Give the extent of all Plasmodium falciparum-infected red blood cells.
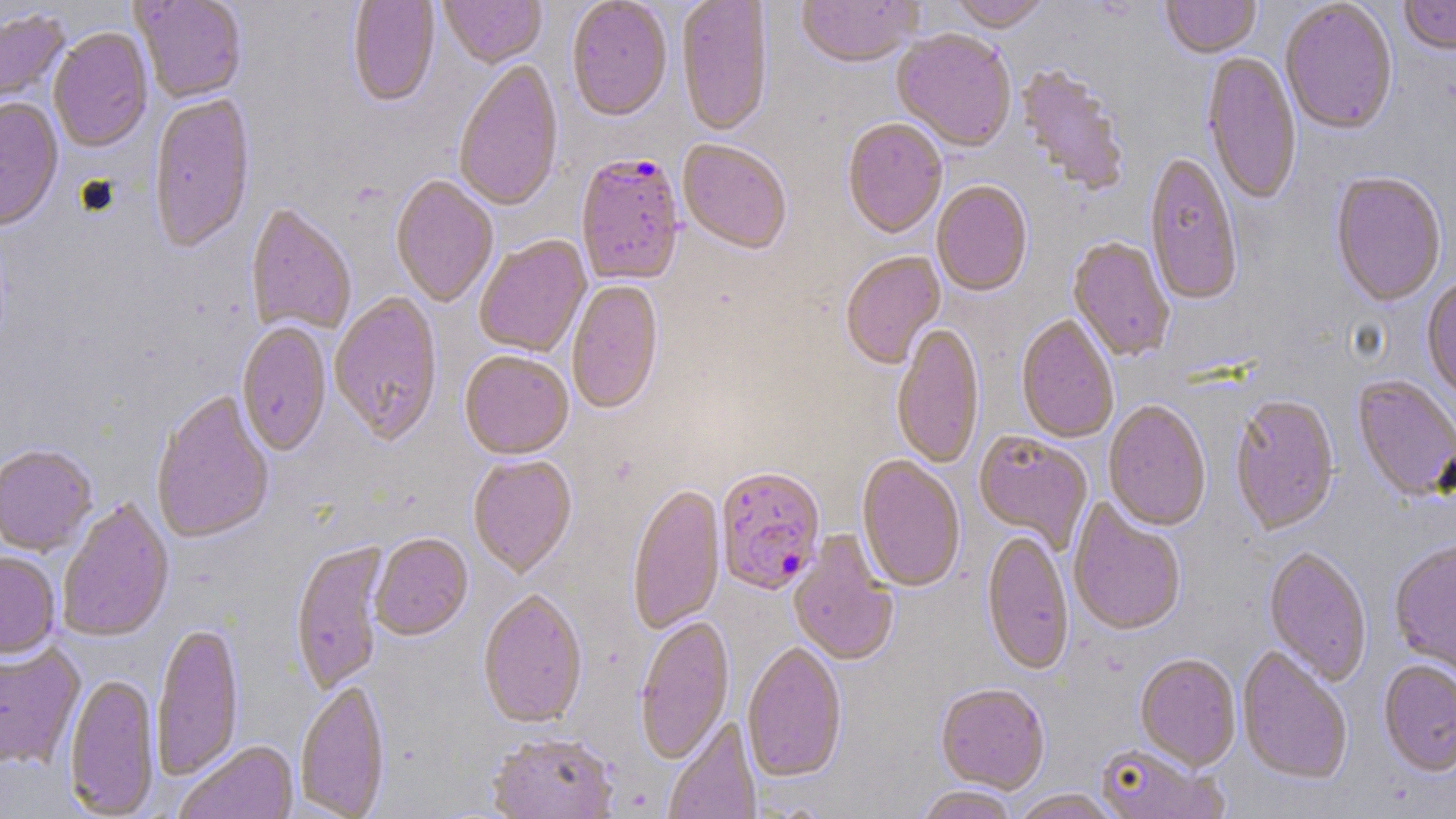
Approximate bounding boxes as named x1/y1/x2/y2 corners in pixels.
Plasmodium falciparum-infected red blood cells: (x1=575, y1=155, x2=685, y2=288), (x1=714, y1=469, x2=826, y2=598).

Uninfected red blood cell locations: (x1=131, y1=0, x2=247, y2=105), (x1=347, y1=0, x2=440, y2=109), (x1=439, y1=0, x2=546, y2=70), (x1=566, y1=0, x2=672, y2=124), (x1=676, y1=0, x2=774, y2=139), (x1=795, y1=0, x2=923, y2=71), (x1=949, y1=0, x2=1052, y2=35), (x1=1161, y1=0, x2=1261, y2=60), (x1=1399, y1=0, x2=1456, y2=57), (x1=1280, y1=2, x2=1398, y2=138), (x1=0, y1=7, x2=71, y2=116), (x1=48, y1=30, x2=153, y2=154), (x1=891, y1=31, x2=1016, y2=153), (x1=1201, y1=53, x2=1301, y2=208), (x1=454, y1=61, x2=564, y2=213), (x1=1014, y1=65, x2=1131, y2=199), (x1=148, y1=96, x2=255, y2=256), (x1=0, y1=99, x2=63, y2=236), (x1=842, y1=119, x2=947, y2=240), (x1=677, y1=140, x2=792, y2=256), (x1=1144, y1=153, x2=1242, y2=308), (x1=1330, y1=173, x2=1447, y2=309), (x1=390, y1=176, x2=498, y2=309), (x1=931, y1=182, x2=1033, y2=298), (x1=245, y1=205, x2=356, y2=336), (x1=475, y1=236, x2=592, y2=358), (x1=1067, y1=238, x2=1174, y2=362), (x1=840, y1=252, x2=946, y2=370), (x1=1421, y1=279, x2=1456, y2=403), (x1=567, y1=280, x2=664, y2=417), (x1=329, y1=294, x2=443, y2=447), (x1=1016, y1=316, x2=1118, y2=445), (x1=236, y1=323, x2=332, y2=458), (x1=891, y1=323, x2=985, y2=470), (x1=459, y1=353, x2=574, y2=462), (x1=1352, y1=376, x2=1456, y2=504), (x1=151, y1=391, x2=275, y2=546), (x1=1229, y1=397, x2=1340, y2=538), (x1=1103, y1=402, x2=1211, y2=533), (x1=973, y1=431, x2=1093, y2=553), (x1=0, y1=446, x2=97, y2=558), (x1=468, y1=456, x2=578, y2=579), (x1=856, y1=456, x2=966, y2=594), (x1=626, y1=485, x2=727, y2=636), (x1=1067, y1=499, x2=1186, y2=638), (x1=57, y1=500, x2=175, y2=644), (x1=788, y1=530, x2=900, y2=668), (x1=982, y1=531, x2=1073, y2=678), (x1=370, y1=534, x2=473, y2=642), (x1=290, y1=540, x2=388, y2=696), (x1=1389, y1=541, x2=1456, y2=679), (x1=1263, y1=547, x2=1372, y2=687), (x1=0, y1=552, x2=61, y2=662), (x1=478, y1=590, x2=588, y2=730), (x1=634, y1=617, x2=735, y2=765), (x1=152, y1=622, x2=244, y2=783), (x1=0, y1=642, x2=86, y2=770), (x1=742, y1=643, x2=847, y2=783), (x1=1237, y1=647, x2=1353, y2=786), (x1=1135, y1=654, x2=1241, y2=772), (x1=1378, y1=661, x2=1456, y2=779), (x1=64, y1=674, x2=161, y2=817), (x1=294, y1=682, x2=391, y2=819), (x1=935, y1=685, x2=1050, y2=795), (x1=663, y1=716, x2=762, y2=819), (x1=486, y1=734, x2=620, y2=819), (x1=175, y1=742, x2=299, y2=819), (x1=1095, y1=742, x2=1228, y2=818), (x1=914, y1=787, x2=1019, y2=819), (x1=1012, y1=790, x2=1120, y2=819). Slide-level diagnosis: Plasmodium falciparum. Thin blood film. 1000x magnification. One field of a larger specimen. Image is 1456×819 pixels. Optical microscopy. May-Grünwald-Giemsa stain.